State the blood parasite species.
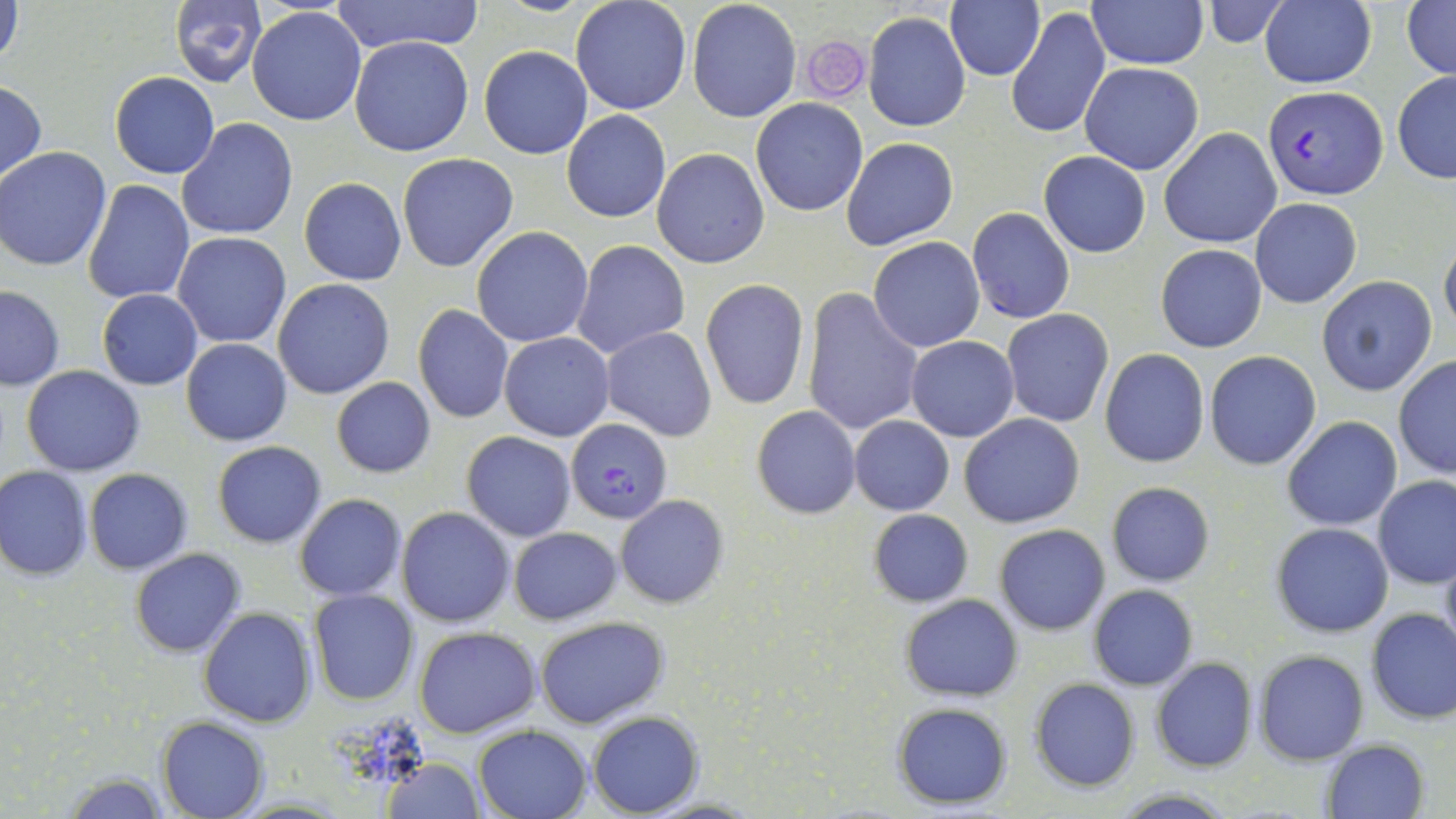

Plasmodium falciparum.

Approximate bounding boxes as named x1/y1/x2/y2 corners in pixels. Plasmodium falciparum-infected red blood cell locations: (x1=1264, y1=87, x2=1387, y2=199), (x1=565, y1=418, x2=671, y2=524). Uninfected red blood cell locations: (x1=1, y1=0, x2=25, y2=77), (x1=168, y1=0, x2=267, y2=87), (x1=328, y1=0, x2=488, y2=53), (x1=570, y1=0, x2=692, y2=116), (x1=687, y1=0, x2=802, y2=123), (x1=945, y1=0, x2=1044, y2=82), (x1=1087, y1=0, x2=1207, y2=68), (x1=1260, y1=0, x2=1376, y2=89), (x1=1203, y1=1, x2=1289, y2=46), (x1=1403, y1=1, x2=1456, y2=80), (x1=1006, y1=6, x2=1109, y2=140), (x1=248, y1=7, x2=367, y2=126), (x1=865, y1=11, x2=971, y2=132), (x1=349, y1=37, x2=473, y2=155), (x1=479, y1=46, x2=591, y2=160), (x1=1079, y1=62, x2=1202, y2=174), (x1=111, y1=71, x2=219, y2=177), (x1=1392, y1=71, x2=1456, y2=183), (x1=0, y1=81, x2=46, y2=187), (x1=751, y1=98, x2=866, y2=216), (x1=561, y1=110, x2=672, y2=223), (x1=178, y1=118, x2=298, y2=240), (x1=1158, y1=128, x2=1282, y2=248), (x1=842, y1=136, x2=958, y2=250), (x1=0, y1=146, x2=113, y2=272), (x1=652, y1=147, x2=770, y2=269), (x1=1039, y1=151, x2=1151, y2=257), (x1=396, y1=153, x2=517, y2=272), (x1=299, y1=177, x2=406, y2=285), (x1=82, y1=180, x2=196, y2=303), (x1=1249, y1=197, x2=1363, y2=308), (x1=967, y1=207, x2=1075, y2=323), (x1=471, y1=227, x2=594, y2=347), (x1=173, y1=231, x2=292, y2=348), (x1=1439, y1=234, x2=1456, y2=339), (x1=869, y1=237, x2=985, y2=353), (x1=570, y1=238, x2=691, y2=358), (x1=1156, y1=244, x2=1267, y2=352), (x1=1315, y1=275, x2=1437, y2=396), (x1=273, y1=277, x2=395, y2=398), (x1=701, y1=281, x2=810, y2=410), (x1=0, y1=286, x2=65, y2=391), (x1=96, y1=289, x2=202, y2=391), (x1=800, y1=290, x2=923, y2=436), (x1=411, y1=303, x2=515, y2=424), (x1=1001, y1=308, x2=1114, y2=427), (x1=600, y1=326, x2=717, y2=442), (x1=499, y1=331, x2=614, y2=442), (x1=905, y1=335, x2=1019, y2=442), (x1=181, y1=337, x2=292, y2=447), (x1=1100, y1=348, x2=1209, y2=468), (x1=1204, y1=350, x2=1321, y2=469), (x1=1394, y1=357, x2=1456, y2=479), (x1=22, y1=364, x2=145, y2=476), (x1=330, y1=376, x2=437, y2=479), (x1=752, y1=406, x2=861, y2=518), (x1=959, y1=413, x2=1084, y2=528), (x1=848, y1=416, x2=954, y2=514), (x1=1282, y1=416, x2=1401, y2=531), (x1=461, y1=430, x2=576, y2=541), (x1=212, y1=440, x2=326, y2=548), (x1=0, y1=466, x2=92, y2=581), (x1=84, y1=468, x2=194, y2=575), (x1=1374, y1=476, x2=1456, y2=588), (x1=1105, y1=481, x2=1216, y2=588), (x1=294, y1=493, x2=407, y2=601), (x1=615, y1=495, x2=729, y2=608), (x1=396, y1=506, x2=515, y2=628), (x1=869, y1=508, x2=973, y2=607), (x1=1271, y1=522, x2=1394, y2=637), (x1=994, y1=524, x2=1110, y2=635), (x1=508, y1=526, x2=621, y2=625), (x1=1438, y1=544, x2=1456, y2=662), (x1=130, y1=548, x2=244, y2=658), (x1=1089, y1=585, x2=1197, y2=690), (x1=308, y1=589, x2=419, y2=706), (x1=900, y1=593, x2=1023, y2=702), (x1=198, y1=606, x2=318, y2=728), (x1=1365, y1=607, x2=1456, y2=726), (x1=534, y1=616, x2=669, y2=729), (x1=413, y1=626, x2=541, y2=738), (x1=1254, y1=649, x2=1368, y2=765), (x1=1152, y1=657, x2=1258, y2=772), (x1=1029, y1=678, x2=1140, y2=791), (x1=891, y1=702, x2=1013, y2=808), (x1=586, y1=710, x2=702, y2=817), (x1=156, y1=716, x2=269, y2=818), (x1=473, y1=726, x2=592, y2=819), (x1=1322, y1=738, x2=1431, y2=818), (x1=380, y1=759, x2=485, y2=816), (x1=58, y1=770, x2=172, y2=818). Platelet locations: (x1=798, y1=34, x2=872, y2=103). One field of a larger specimen. Thin blood smear. 1000x magnification. Image is 1456×819 pixels. May-Grünwald-Giemsa-stained preparation. Optical microscopy.